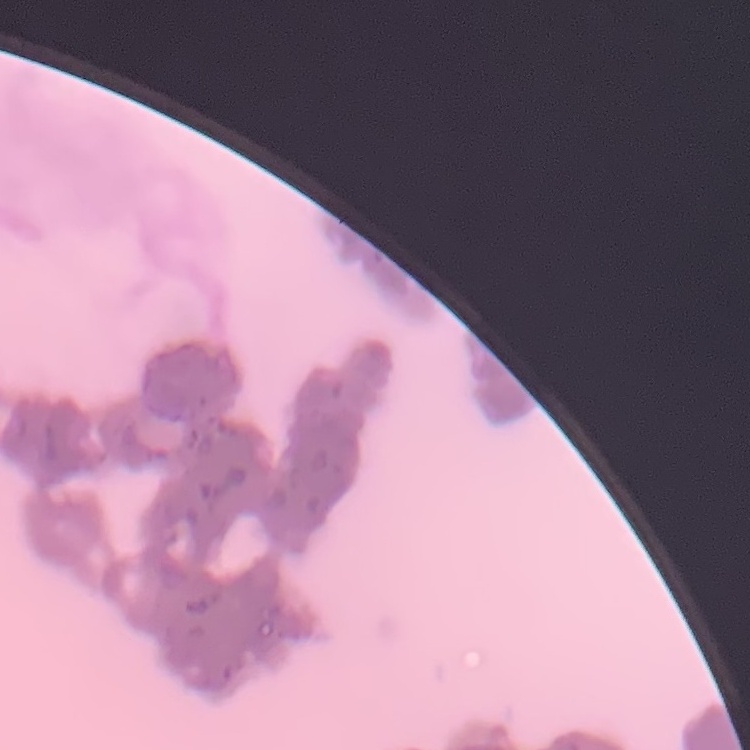

Summary:
  - Red blood cell morphology: rouleaux formation
  - Image type: square crop of a larger photomicrograph
  - Stain: Field's or Giemsa
  - Preparation: thin peripheral smear